Assess this cell for malaria.
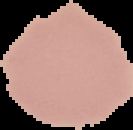
Uninfected.

{
  "image_type": "segmented cell region with the area outside set to black",
  "image_size": "133×130 pixels",
  "preparation": "thin blood film"
}